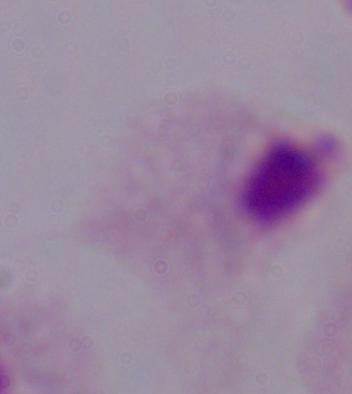
modality = micrograph
identification = trichomonad
magnification = 1000x